Outline each Plasmodium falciparum-infected red blood cell.
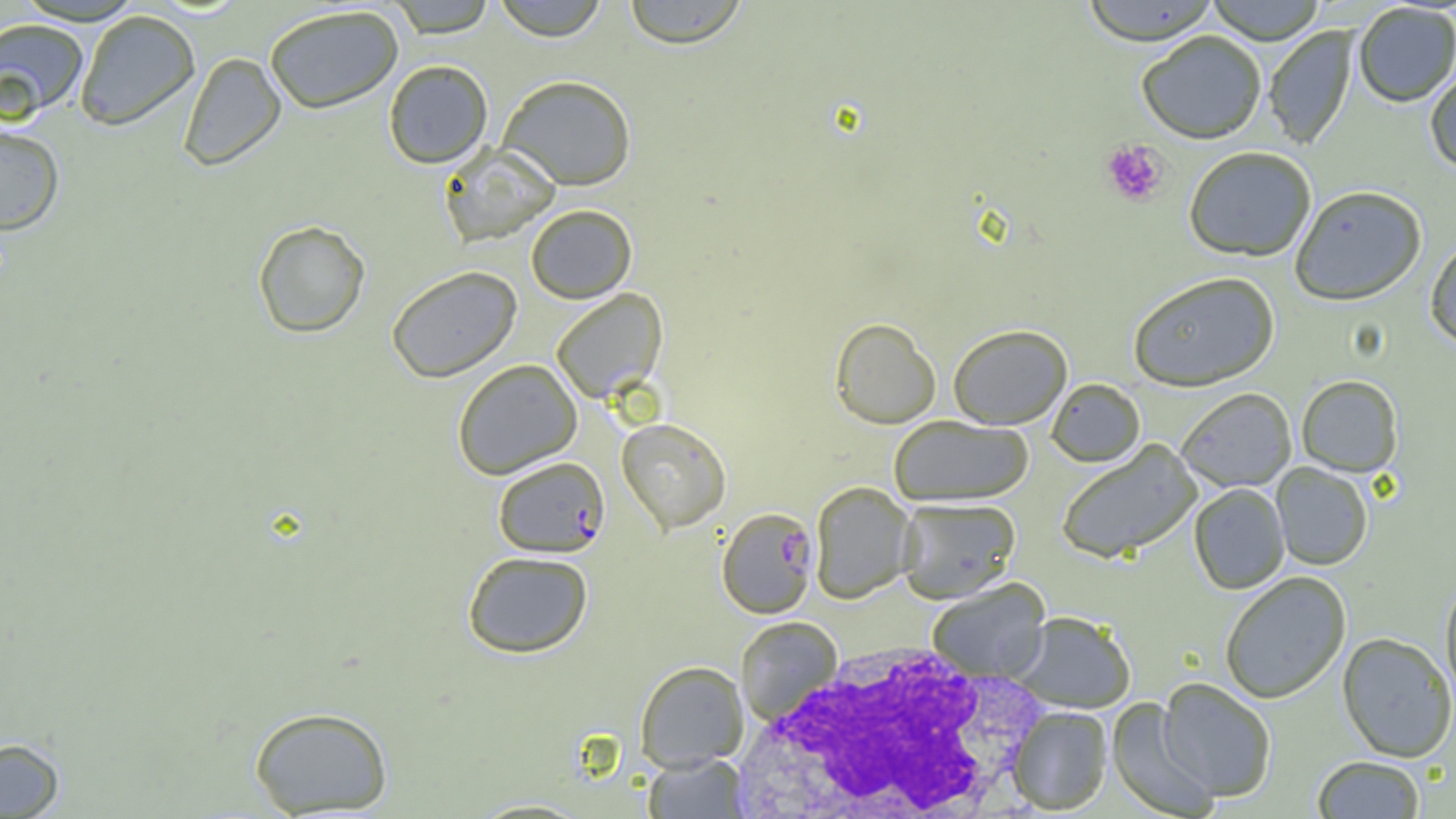

Approximate bounding boxes as (x1, y1, x2, y2) in pixels.
Plasmodium falciparum-infected red blood cells: (493, 456, 610, 557), (717, 507, 819, 619).

White blood cell locations: (722, 638, 1059, 819). Uninfected red blood cell locations: (13, 0, 145, 25), (389, 0, 497, 37), (491, 0, 609, 41), (621, 0, 749, 48), (1079, 0, 1221, 45), (1205, 0, 1327, 44), (1353, 3, 1456, 107), (263, 4, 404, 114), (74, 9, 200, 130), (0, 18, 90, 121), (1263, 26, 1358, 151), (1136, 30, 1267, 144), (179, 52, 286, 171), (383, 59, 493, 168), (1424, 63, 1456, 175), (498, 74, 637, 190), (0, 122, 65, 234), (439, 144, 560, 247), (1183, 146, 1317, 262), (1289, 185, 1427, 306), (526, 204, 637, 303), (253, 220, 370, 338), (1425, 237, 1456, 353), (387, 266, 521, 382), (1128, 271, 1280, 392), (550, 288, 667, 403), (830, 317, 941, 429), (947, 324, 1073, 429), (452, 358, 582, 479), (1296, 375, 1403, 477), (1046, 379, 1145, 468), (1177, 388, 1297, 492), (889, 415, 1033, 506), (616, 417, 731, 533), (1056, 440, 1202, 564), (1270, 463, 1373, 571), (809, 481, 916, 604), (1188, 483, 1290, 594), (896, 497, 1021, 603), (462, 550, 593, 658), (1219, 571, 1352, 704), (1439, 574, 1456, 708), (926, 579, 1051, 683), (1010, 611, 1137, 713), (736, 616, 842, 725), (1337, 632, 1455, 763), (635, 660, 749, 770), (1157, 678, 1276, 803), (1106, 698, 1219, 819), (248, 706, 394, 816), (1008, 706, 1112, 815), (0, 737, 65, 818), (643, 753, 748, 818), (1312, 756, 1425, 818). Platelet locations: (1101, 139, 1169, 206). Slide-level diagnosis: Plasmodium falciparum. 1000x magnification. Optical microscopy. Thin blood smear. One field of a larger specimen. Image is 1456×819 pixels.